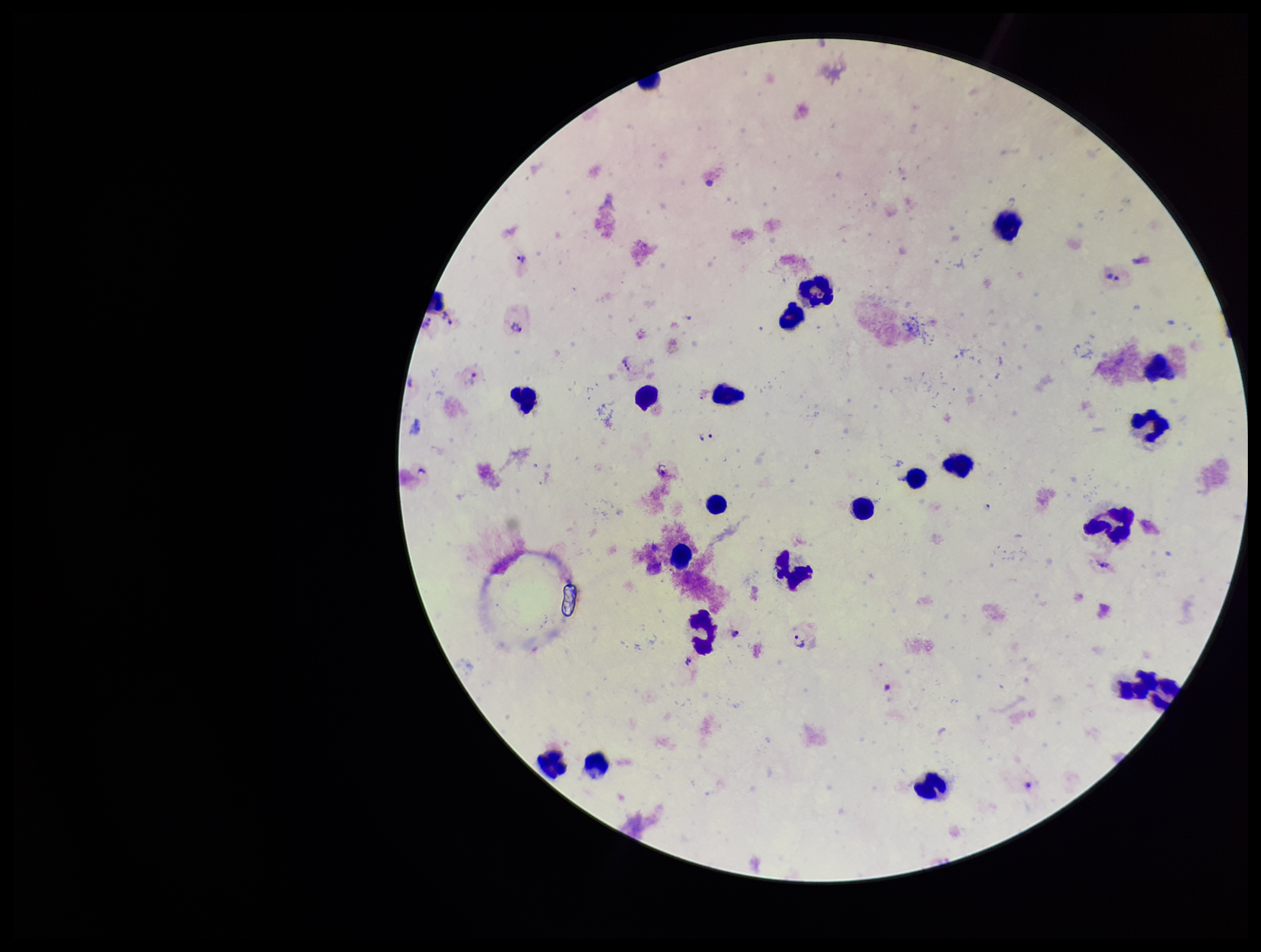
Species reported for this patient: Plasmodium vivax. Leukocyte count: 21. Plasmodium parasites: seen. One field from this slide. Preparation: thick blood smear. Image is 1261×952 pixels. Giemsa stain. Patient malaria status: infected. Parasite count: 5. Photographed through the microscope eyepiece with a smartphone camera.